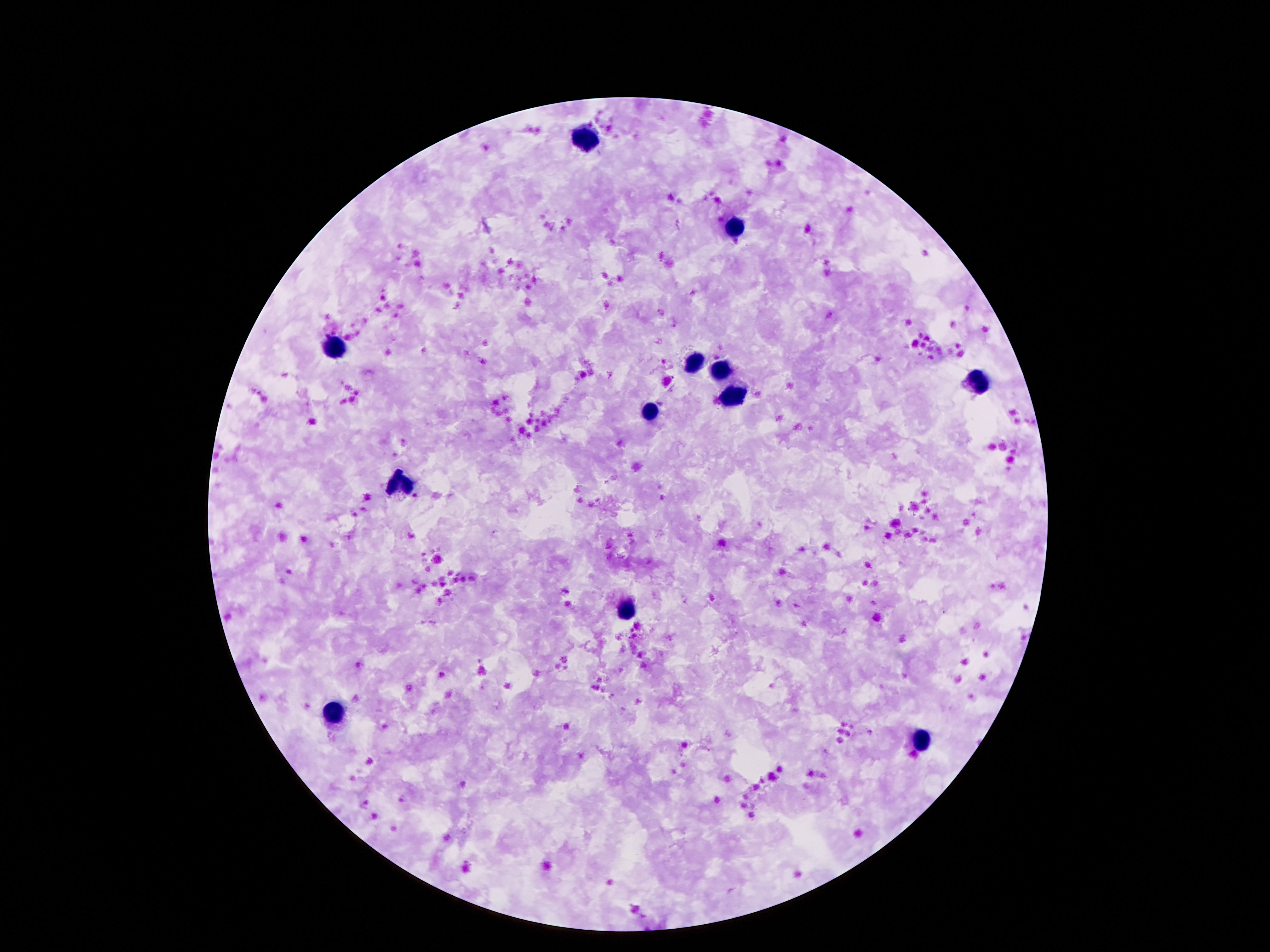

Approximate centers as {x, y} in pixels.
Summary:
  - Leukocyte locations: {588, 139}, {738, 228}, {335, 351}, {693, 362}, {723, 371}, {979, 383}, {734, 400}, {653, 414}, {403, 487}, {628, 611}, {333, 714}, {923, 742}
  - Image size: 1270×952 pixels
  - Magnification: 100x
  - Capture: smartphone camera through the microscope eyepiece
  - Stain: Giemsa
  - Preparation: thick blood smear
  - Field of view: single
  - Patient malaria status: negative